Describe the morphology of the erythrocytes.
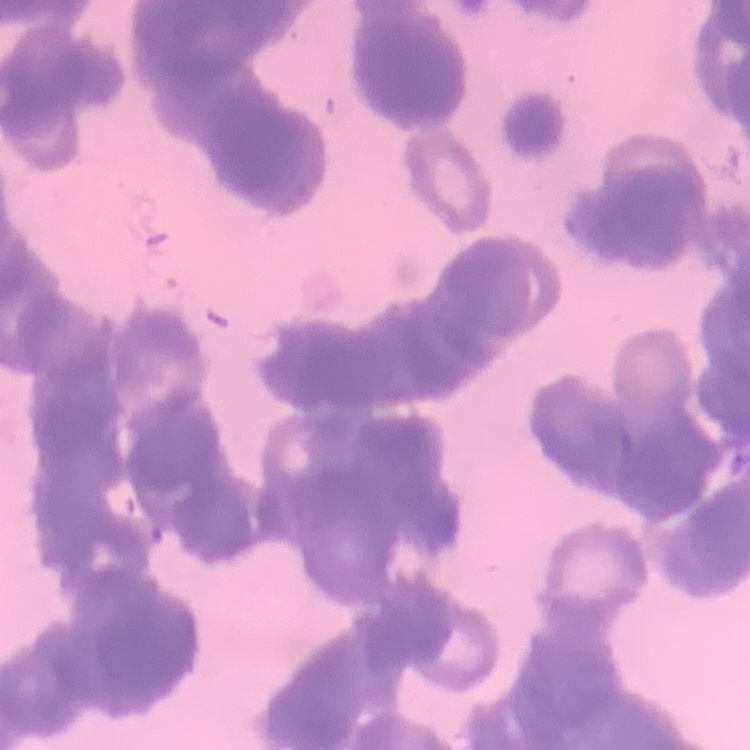
They show rouleaux formation.

image type = one tile cut from a larger photomicrograph
preparation = thin blood smear
stain = Field's or Giemsa